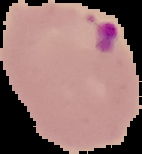

Summary:
  - Preparation: thin blood smear
  - Image type: cell region segmented out of the field of view; surrounding area masked to black
  - Malaria status: parasitized
  - Image size: 142×154 pixels